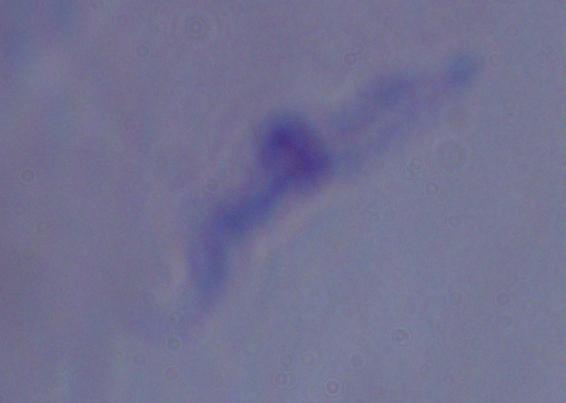

Summary:
  - Magnification: 1000x
  - Identification: trypanosome
  - Modality: photomicrograph